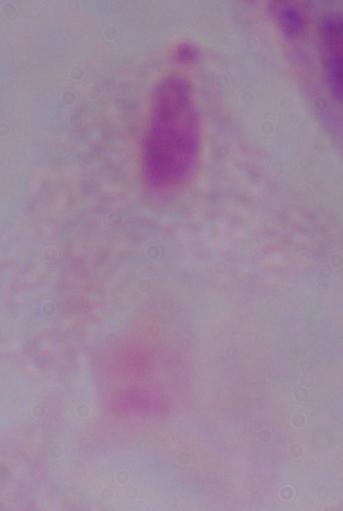 Micrograph. 1000x magnification. A trichomonad is seen.